Assess this cell for malaria.
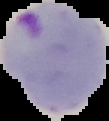

It is parasitized.

Segmented cell region on a black background. Image is 109×121 pixels. From a thin blood film.